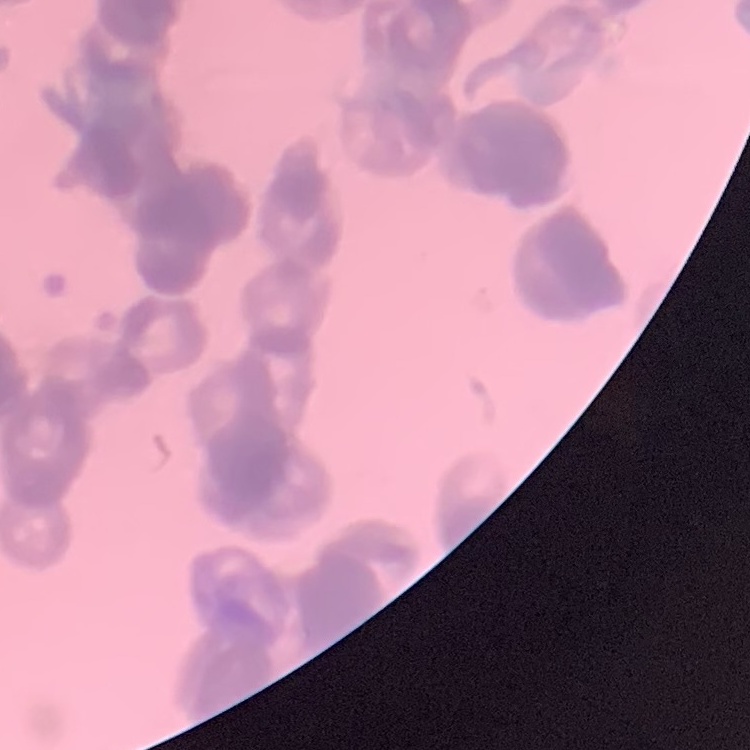
Summary:
  - Red blood cell morphology: rouleaux formation
  - Stain: Field's or Giemsa
  - Image type: square crop of a larger photomicrograph
  - Preparation: thin blood smear